Look for Plasmodium parasites.
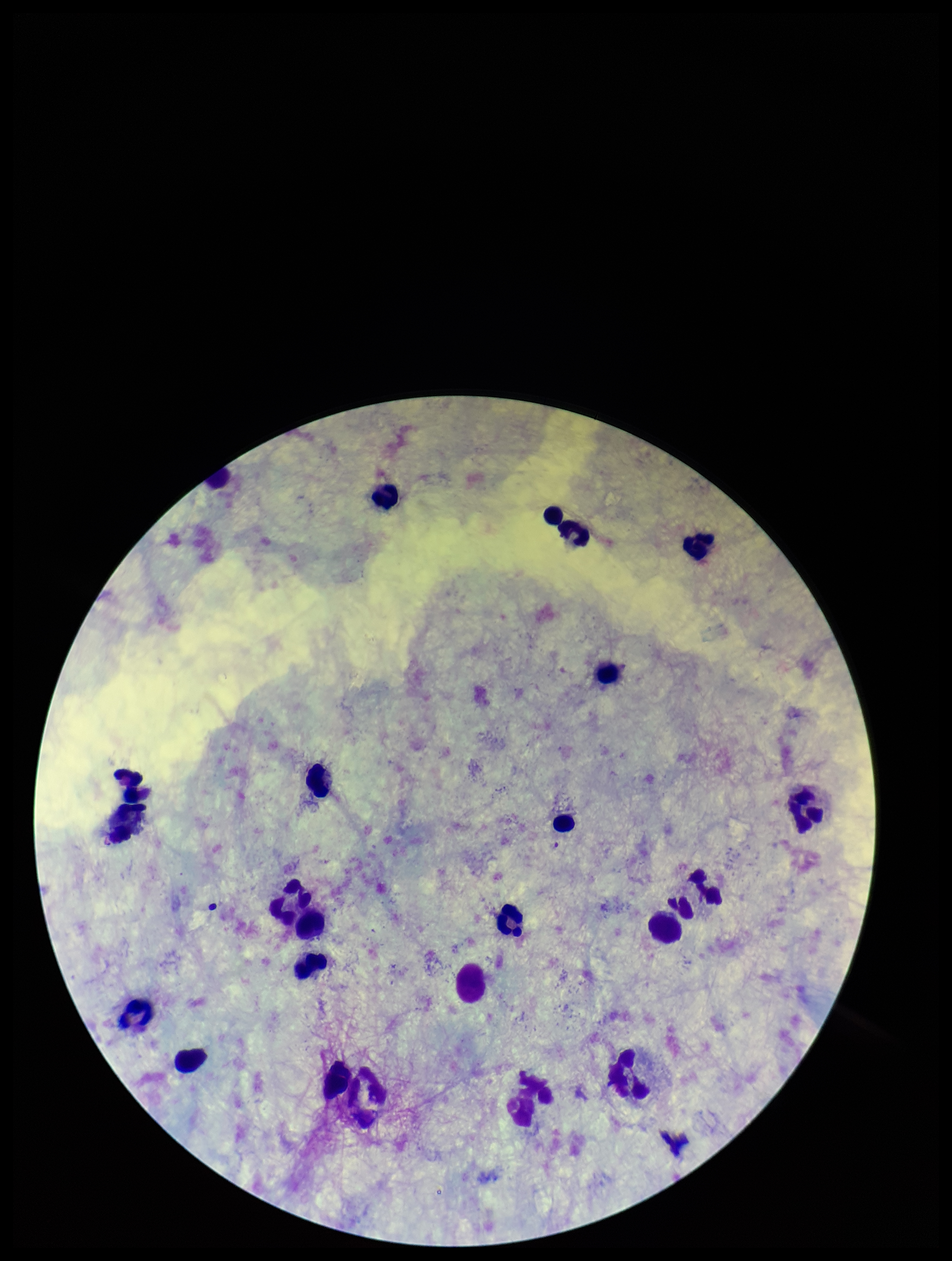

None seen.

One field from this slide. Patient malaria status: negative. Parasite count: 0. Preparation: thick. Smartphone photograph taken through the eyepiece of a microscope. Giemsa stain. Leukocyte count: 24. Image is 952×1261 pixels.